Name the cell type shown.
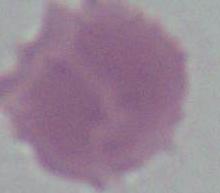
This is an erythrocyte.

Summary:
  - Modality: micrograph
  - Magnification: 1000x